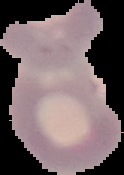
image_size: 124×175 pixels
image_type: segmented cell region on a black background
malaria_status: parasitized
preparation: thin blood film